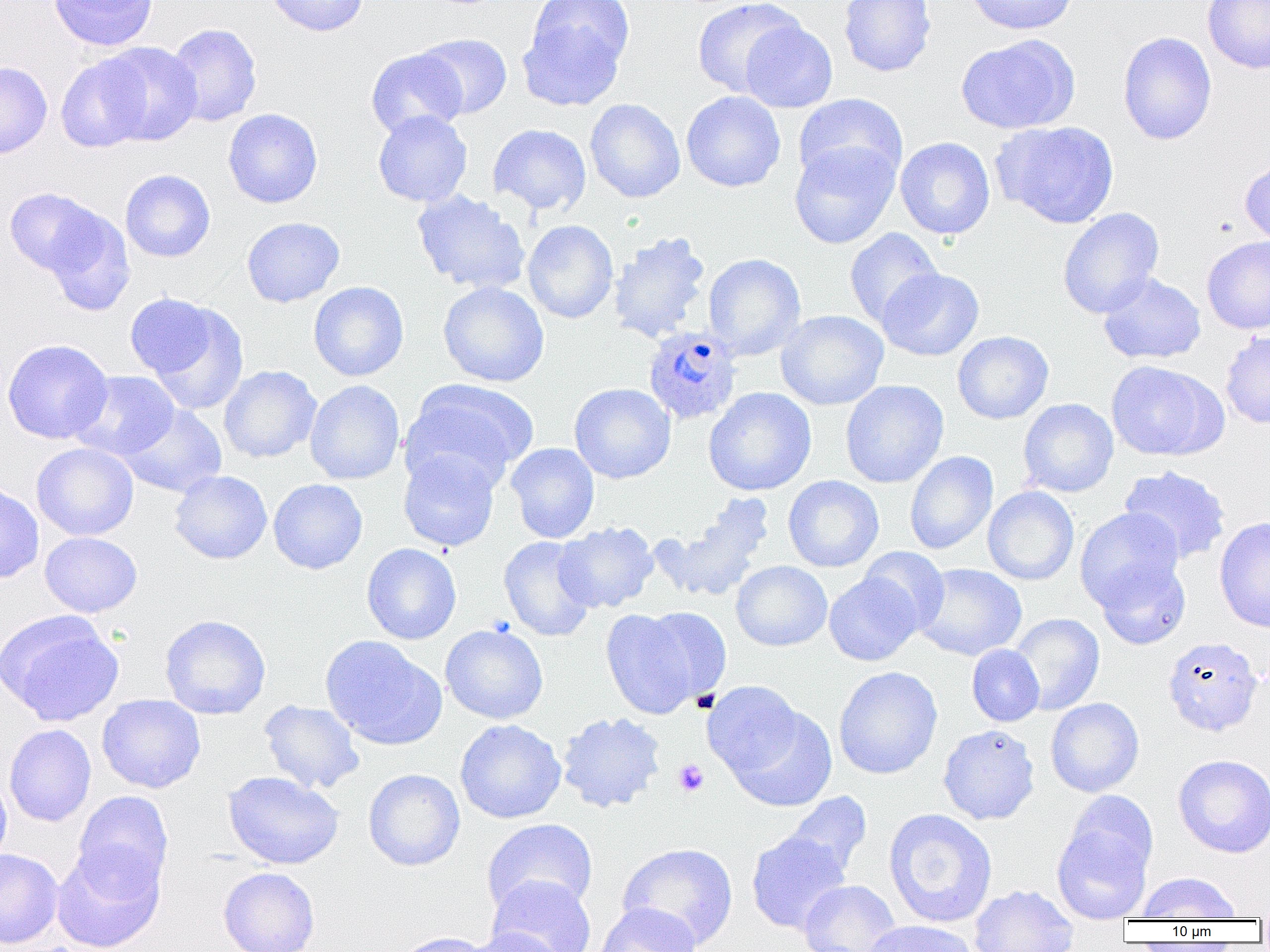

Summary:
  - Coordinate format: approximate bounding boxes as named x1/y1/x2/y2 corners in pixels
  - Uninfected red blood cell locations: (x1=49, y1=0, x2=158, y2=51), (x1=264, y1=0, x2=370, y2=36), (x1=692, y1=0, x2=805, y2=99), (x1=838, y1=0, x2=936, y2=77), (x1=965, y1=0, x2=1077, y2=34), (x1=1202, y1=1, x2=1270, y2=74), (x1=518, y1=8, x2=631, y2=110), (x1=740, y1=20, x2=837, y2=113), (x1=165, y1=23, x2=263, y2=126), (x1=1117, y1=31, x2=1217, y2=145), (x1=415, y1=33, x2=512, y2=119), (x1=956, y1=34, x2=1079, y2=135), (x1=98, y1=42, x2=202, y2=146), (x1=367, y1=48, x2=466, y2=139), (x1=56, y1=54, x2=152, y2=152), (x1=0, y1=62, x2=52, y2=159), (x1=681, y1=91, x2=785, y2=192), (x1=793, y1=93, x2=907, y2=189), (x1=584, y1=99, x2=685, y2=203), (x1=223, y1=108, x2=323, y2=208), (x1=372, y1=110, x2=473, y2=207), (x1=994, y1=120, x2=1119, y2=229), (x1=488, y1=123, x2=591, y2=215), (x1=895, y1=137, x2=995, y2=240), (x1=789, y1=140, x2=900, y2=249), (x1=1240, y1=157, x2=1270, y2=248), (x1=120, y1=169, x2=216, y2=262), (x1=4, y1=188, x2=105, y2=277), (x1=411, y1=189, x2=532, y2=295), (x1=1058, y1=207, x2=1164, y2=319), (x1=43, y1=208, x2=135, y2=316), (x1=241, y1=216, x2=345, y2=307), (x1=522, y1=220, x2=618, y2=324), (x1=844, y1=228, x2=943, y2=328), (x1=608, y1=231, x2=711, y2=344), (x1=1202, y1=235, x2=1270, y2=334), (x1=703, y1=253, x2=806, y2=361), (x1=877, y1=268, x2=984, y2=361), (x1=1098, y1=272, x2=1206, y2=364), (x1=309, y1=281, x2=409, y2=381), (x1=438, y1=281, x2=549, y2=387), (x1=124, y1=294, x2=216, y2=377), (x1=148, y1=303, x2=248, y2=416), (x1=776, y1=310, x2=888, y2=410), (x1=952, y1=331, x2=1053, y2=424), (x1=1220, y1=331, x2=1270, y2=429), (x1=2, y1=339, x2=113, y2=444), (x1=1106, y1=360, x2=1221, y2=461), (x1=219, y1=365, x2=321, y2=463), (x1=70, y1=370, x2=180, y2=461), (x1=400, y1=379, x2=538, y2=491), (x1=305, y1=380, x2=405, y2=485), (x1=840, y1=380, x2=949, y2=488), (x1=569, y1=382, x2=676, y2=484), (x1=703, y1=387, x2=816, y2=496), (x1=1018, y1=398, x2=1118, y2=498), (x1=119, y1=403, x2=227, y2=498), (x1=31, y1=442, x2=138, y2=540), (x1=505, y1=442, x2=600, y2=544), (x1=398, y1=449, x2=501, y2=552), (x1=905, y1=451, x2=998, y2=555), (x1=1119, y1=466, x2=1231, y2=565), (x1=169, y1=470, x2=272, y2=564), (x1=783, y1=475, x2=884, y2=572), (x1=268, y1=478, x2=368, y2=574), (x1=0, y1=482, x2=44, y2=584), (x1=982, y1=486, x2=1079, y2=585), (x1=654, y1=498, x2=773, y2=602), (x1=1074, y1=507, x2=1184, y2=610), (x1=1214, y1=516, x2=1270, y2=633), (x1=554, y1=521, x2=659, y2=613), (x1=40, y1=532, x2=142, y2=617), (x1=499, y1=535, x2=596, y2=641), (x1=361, y1=542, x2=461, y2=644), (x1=858, y1=547, x2=950, y2=633), (x1=1095, y1=559, x2=1191, y2=649), (x1=731, y1=560, x2=832, y2=651), (x1=913, y1=563, x2=1027, y2=661), (x1=824, y1=573, x2=921, y2=666), (x1=640, y1=606, x2=732, y2=703), (x1=599, y1=608, x2=706, y2=718), (x1=1, y1=611, x2=123, y2=726), (x1=1007, y1=613, x2=1105, y2=715), (x1=160, y1=614, x2=271, y2=719), (x1=440, y1=623, x2=549, y2=724), (x1=320, y1=635, x2=446, y2=749), (x1=1163, y1=635, x2=1264, y2=735), (x1=967, y1=644, x2=1044, y2=727), (x1=834, y1=666, x2=942, y2=780), (x1=702, y1=680, x2=806, y2=780), (x1=97, y1=694, x2=205, y2=793), (x1=1045, y1=697, x2=1145, y2=797), (x1=259, y1=700, x2=364, y2=794), (x1=728, y1=705, x2=838, y2=812), (x1=556, y1=711, x2=666, y2=813), (x1=455, y1=719, x2=566, y2=823), (x1=4, y1=724, x2=97, y2=827), (x1=938, y1=724, x2=1039, y2=825), (x1=1173, y1=754, x2=1270, y2=858), (x1=363, y1=768, x2=465, y2=871), (x1=223, y1=771, x2=344, y2=870), (x1=0, y1=774, x2=12, y2=866), (x1=73, y1=791, x2=174, y2=894), (x1=784, y1=791, x2=872, y2=881), (x1=883, y1=808, x2=997, y2=928), (x1=1052, y1=813, x2=1154, y2=924), (x1=481, y1=819, x2=598, y2=917), (x1=746, y1=831, x2=850, y2=934), (x1=617, y1=842, x2=738, y2=949), (x1=52, y1=844, x2=165, y2=952), (x1=0, y1=848, x2=63, y2=948), (x1=218, y1=866, x2=320, y2=952), (x1=1136, y1=872, x2=1241, y2=921), (x1=487, y1=875, x2=596, y2=952), (x1=798, y1=880, x2=901, y2=952), (x1=969, y1=884, x2=1079, y2=952), (x1=594, y1=901, x2=700, y2=952), (x1=863, y1=920, x2=980, y2=952), (x1=462, y1=928, x2=567, y2=952), (x1=391, y1=932, x2=495, y2=952)
  - Platelet locations: (x1=673, y1=759, x2=709, y2=796)
  - Plasmodium ovale-infected red blood cell locations: (x1=643, y1=327, x2=742, y2=425)
  - Slide-level diagnosis: Plasmodium ovale
  - Image size: 1270×952 pixels
  - Field of view: one of a larger specimen
  - Modality: light microscopy
  - Preparation: thin blood smear
  - Magnification: 1000x